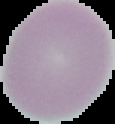
Malaria status: uninfected. Image is 115×124 pixels. From a thin blood film. Cell region segmented out of the field of view; the surrounding area is masked to black.